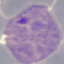

malaria status = parasitized
preparation = thin smear
capture = smartphone through the microscope eyepiece
image type = cell patch, automatically extracted from a larger field of view and resized to 64 × 64 pixels
stain = Giemsa